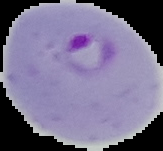
{
  "image_type": "segmented cell region with the area outside set to black",
  "malaria_status": "parasitized",
  "preparation": "thin blood smear",
  "image_size": "163×151 pixels"
}